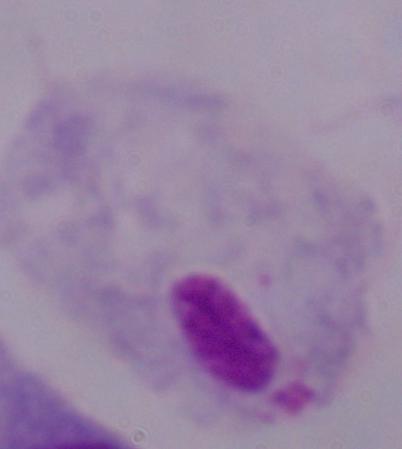
Summary:
  - Modality: micrograph
  - Identification: trichomonad
  - Magnification: 1000x